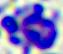

Summary:
  - Magnification: 400x
  - Modality: photomicrograph
  - Identification: leukocyte